Describe the morphology of the erythrocytes.
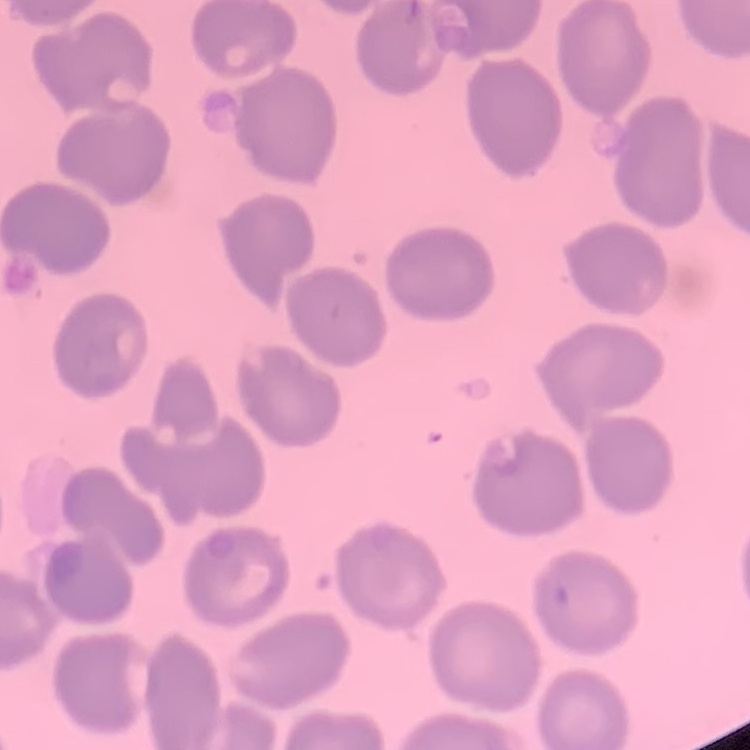

They show no rouleaux formation.

Stained with either Field's or Giemsa. Square crop of a larger photomicrograph. Thin blood smear.